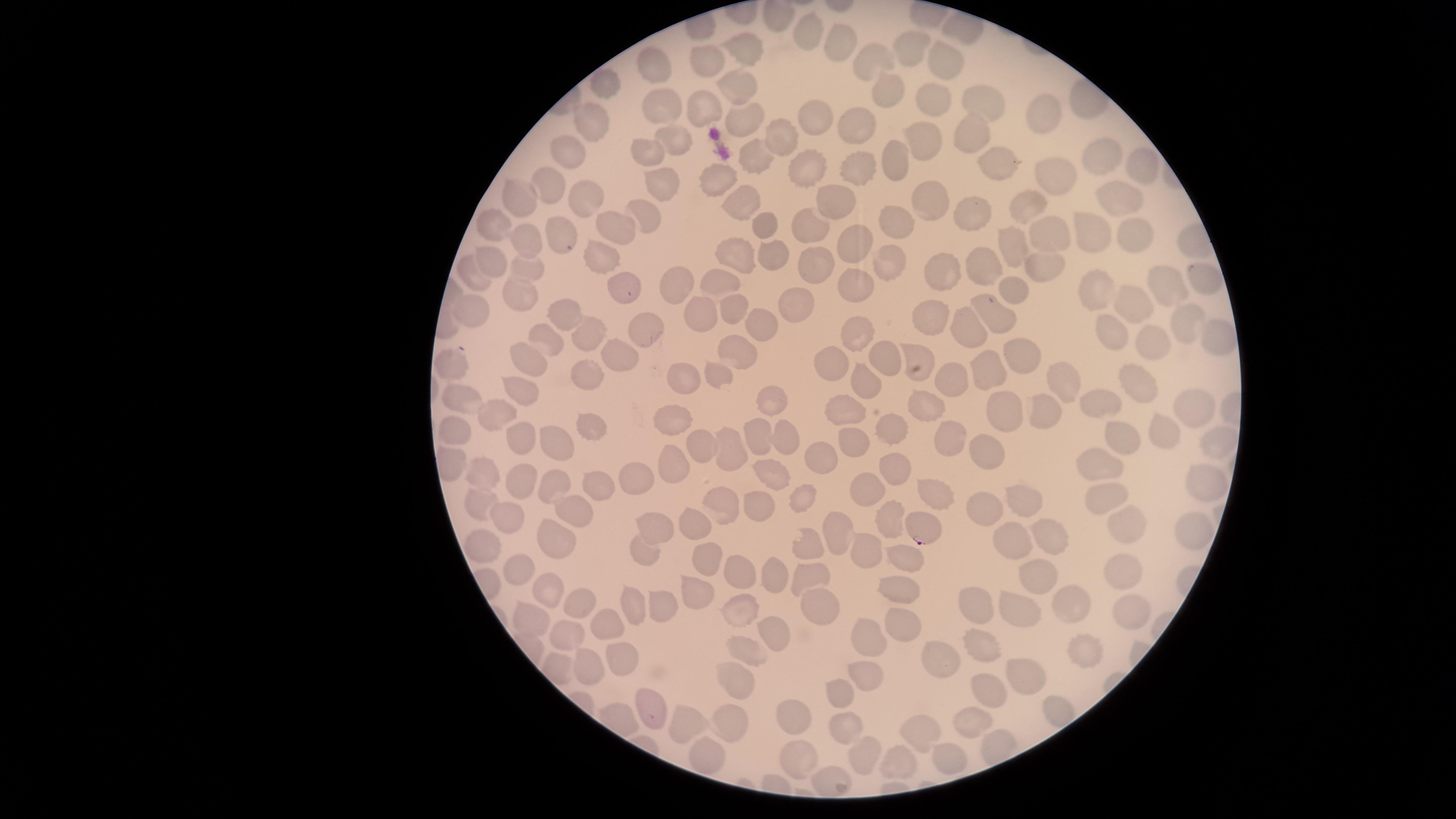
Approximate marker points as (x, y) in pixels. Parasitized red blood cells: (924, 527). Uninfected red blood cells: (807, 32), (838, 46), (745, 49), (914, 50), (873, 57), (947, 59), (708, 66), (650, 69), (606, 82), (739, 83), (889, 90), (980, 97), (663, 99), (934, 102), (702, 109), (746, 117), (1043, 117), (591, 118), (816, 119), (857, 120), (975, 133), (679, 137), (784, 137), (925, 139), (570, 149), (650, 152), (755, 154), (1103, 156), (896, 162), (1139, 163), (997, 165), (806, 168), (858, 168), (1051, 173), (724, 178), (547, 183), (663, 186), (1118, 193), (522, 195), (582, 195), (930, 196), (837, 200), (1031, 203), (744, 204), (968, 212), (644, 216), (763, 222), (903, 222), (494, 225), (615, 226), (560, 229), (807, 229), (1130, 229), (1089, 232), (1048, 233), (851, 238), (525, 240), (1017, 246), (740, 253), (775, 253), (598, 258), (891, 258), (820, 260), (980, 261), (487, 262), (527, 267), (1045, 267), (940, 272), (473, 275), (1198, 275), (724, 280), (670, 283), (855, 283), (1167, 285), (625, 289), (1014, 289), (513, 291), (1096, 293), (1133, 304), (800, 305), (730, 307), (695, 308), (475, 312), (564, 315), (928, 318), (999, 318), (1185, 321), (759, 324), (858, 327), (966, 328), (647, 329), (588, 330), (1108, 330), (1215, 335), (551, 336), (1151, 343), (737, 346), (619, 353), (916, 353), (529, 355), (883, 356), (1021, 356), (835, 362), (456, 366), (987, 367), (587, 372), (684, 375), (1056, 377), (716, 379), (864, 383), (950, 383), (516, 384), (1133, 384), (773, 398), (1105, 398), (467, 401), (926, 405), (1193, 405), (1042, 407), (846, 408), (1008, 408), (500, 413), (675, 416), (1163, 426), (592, 427), (453, 428), (891, 428), (756, 435), (522, 439), (561, 439), (951, 439), (1119, 441), (1205, 441), (704, 442), (781, 442), (848, 442), (986, 447), (727, 451), (822, 454), (1096, 457), (893, 467), (673, 468), (483, 471), (770, 473), (514, 477), (637, 479), (1203, 484), (546, 487), (596, 487), (870, 490), (935, 492), (1103, 495), (804, 496), (1019, 496), (720, 497), (482, 503), (990, 504), (758, 505), (572, 508), (505, 513), (890, 515), (697, 520), (1121, 520), (655, 522), (1187, 524), (834, 530), (1050, 533), (559, 539), (1010, 539), (808, 542), (487, 546), (867, 547), (644, 553), (906, 553), (708, 561), (521, 563), (1122, 567), (809, 569), (1031, 571), (738, 580), (768, 581), (691, 586), (548, 587), (897, 591), (977, 600), (581, 601), (665, 602), (816, 605), (635, 606), (1063, 607), (741, 609), (1022, 609), (1128, 614), (525, 616), (898, 623), (606, 627), (773, 631), (571, 634), (866, 635), (750, 643), (983, 646), (1075, 649), (936, 655), (622, 661), (586, 666), (737, 672), (1022, 676), (869, 678), (841, 688), (990, 690), (645, 712), (792, 713), (842, 718), (973, 718), (731, 723), (691, 724), (915, 732), (858, 748), (712, 750), (946, 759), (898, 761), (794, 764). Smartphone photograph through the microscope eyepiece. One field of view of the specimen. Image is 1456×819 pixels. Species: Plasmodium falciparum. Thin blood smear. Presence: malaria parasites detected. The visible region is circular. Giemsa stain.